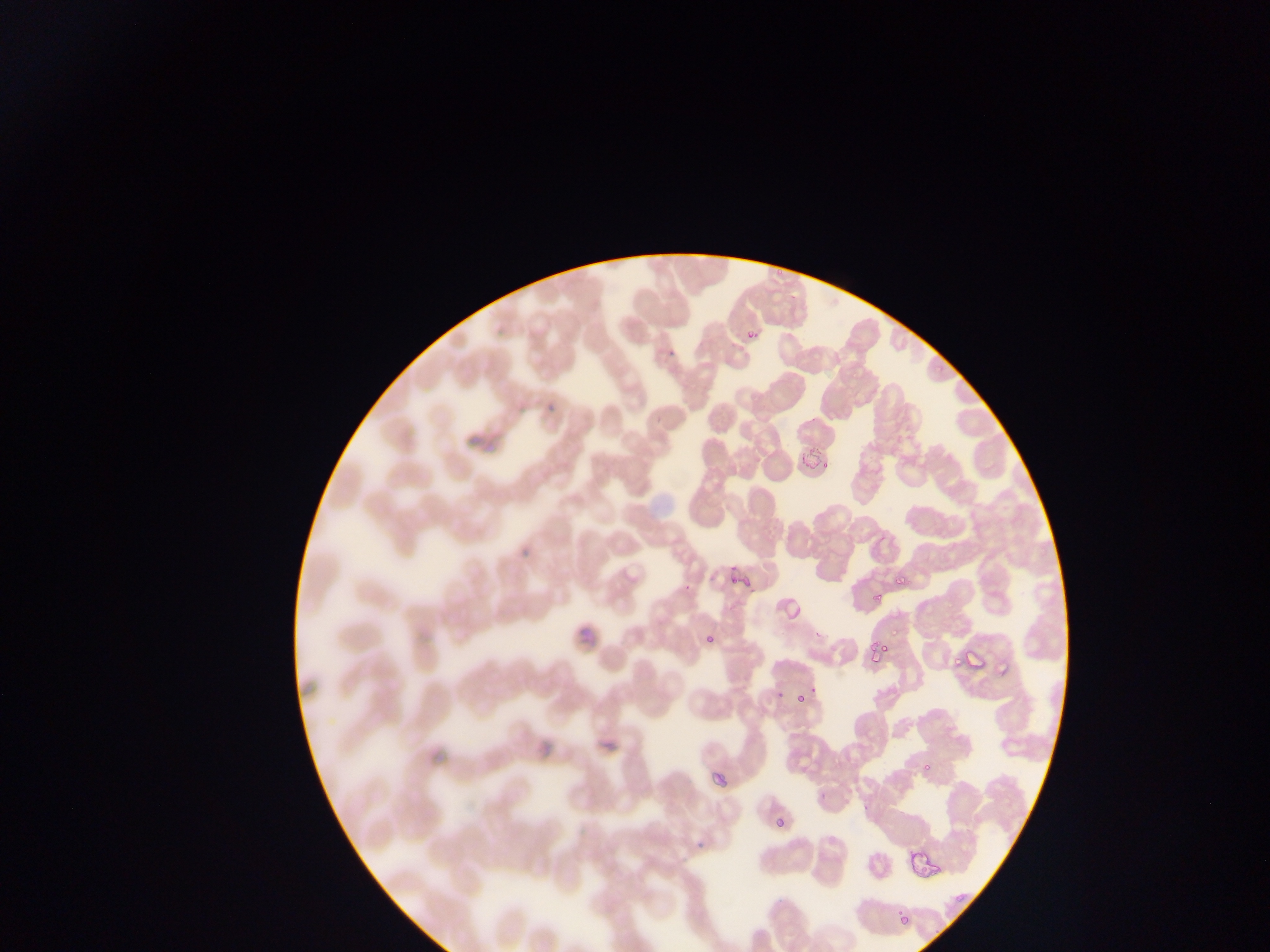
Approximate bounding boxes as (left, top, right, bottom) in pixels. Malaria parasite locations: (745, 324, 761, 339), (724, 563, 743, 587), (894, 577, 908, 589), (889, 626, 902, 635), (703, 629, 716, 644), (868, 639, 890, 663), (970, 646, 984, 668), (953, 653, 971, 665), (793, 691, 809, 703), (916, 760, 938, 777), (712, 770, 726, 787), (774, 818, 787, 828), (949, 884, 970, 906), (896, 910, 915, 927). Thin blood smear. Collected in Ghana. Photographed through a microscope with a mobile-phone camera. Single field of view. Image is 1270×952 pixels.